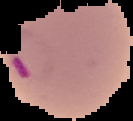
preparation = thin blood smear
malaria status = parasitized
image size = 133×121 pixels
image type = segmented cell region with the area outside set to black